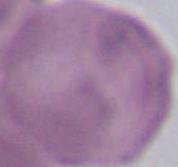
{
  "modality": "photomicrograph",
  "identification": "erythrocyte",
  "magnification": "1000x"
}